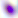
modality = photomicrograph
magnification = 400x
identification = Toxoplasma gondii